Locate every blood parasite and identify its species.
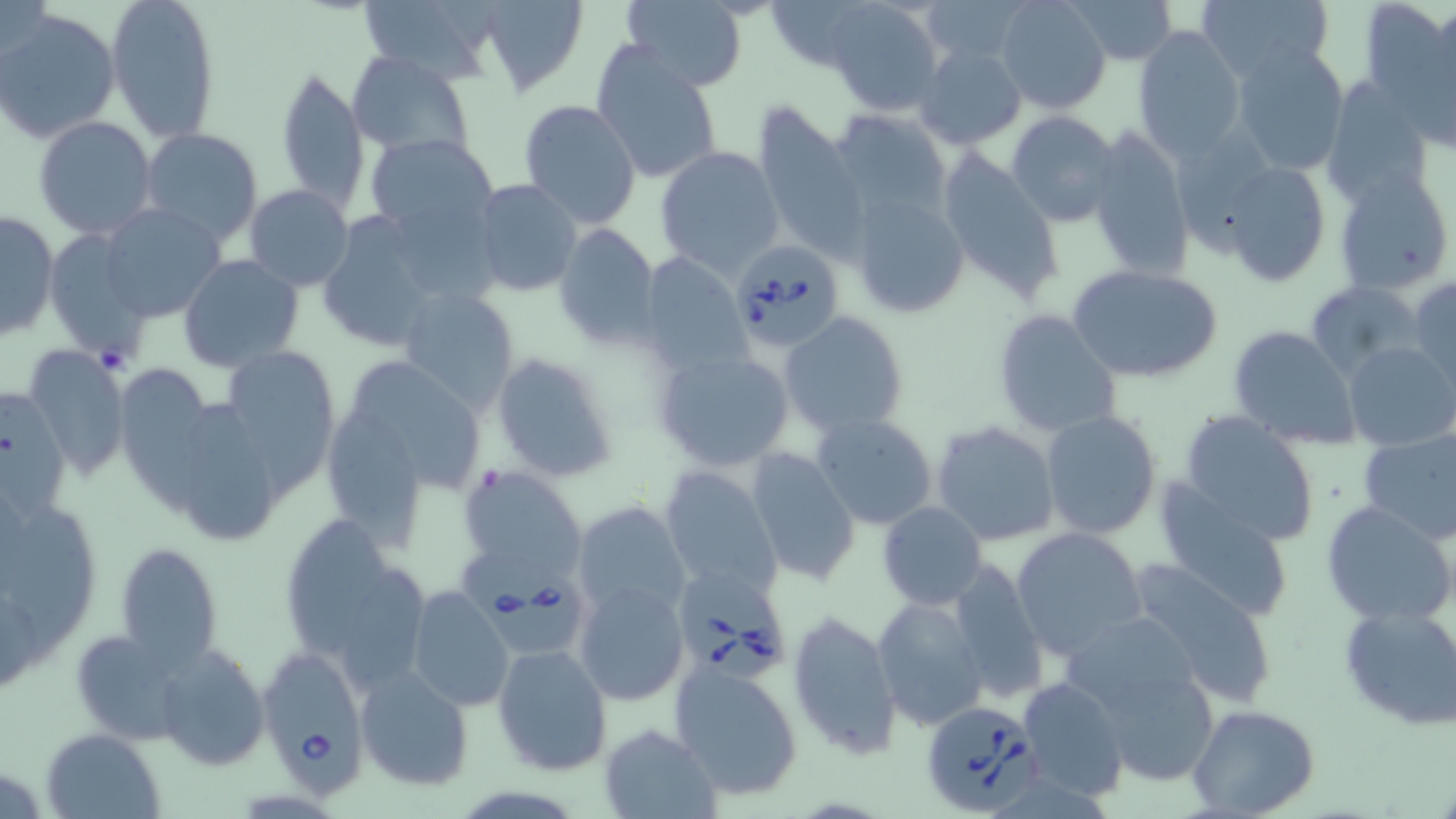
Approximate bounding boxes as (x1, y1, x2, y2) in pixels.
Babesia divergens-infected red blood cells: (733, 238, 844, 350), (460, 551, 604, 658), (680, 575, 790, 678), (257, 641, 372, 801), (919, 699, 1047, 817).
No Plasmodium falciparum, Plasmodium ovale, Plasmodium malariae, Plasmodium vivax, or Trypanosoma brucei observed.

Uninfected red blood cell locations: (0, 0, 56, 70), (105, 0, 221, 142), (357, 0, 496, 81), (476, 0, 588, 95), (618, 0, 751, 91), (761, 0, 881, 72), (918, 0, 1032, 64), (994, 0, 1112, 115), (1070, 0, 1179, 64), (1198, 0, 1335, 86), (1361, 0, 1453, 114), (825, 1, 942, 117), (2, 8, 122, 144), (1133, 27, 1246, 158), (1231, 42, 1352, 176), (591, 43, 723, 186), (915, 43, 1026, 149), (347, 51, 474, 160), (275, 64, 370, 214), (1322, 74, 1433, 205), (518, 100, 640, 229), (750, 101, 869, 260), (831, 106, 951, 218), (1007, 111, 1121, 228), (34, 116, 157, 239), (1086, 124, 1193, 281), (138, 127, 265, 248), (364, 133, 500, 243), (934, 146, 1064, 305), (653, 147, 784, 277), (1220, 159, 1333, 287), (1334, 171, 1454, 295), (472, 180, 583, 299), (244, 184, 354, 291), (847, 189, 971, 318), (99, 203, 226, 322), (313, 208, 473, 352), (1, 211, 60, 342), (552, 222, 662, 351), (41, 228, 153, 363), (638, 251, 752, 377), (178, 254, 304, 372), (1068, 266, 1221, 384), (1408, 276, 1456, 392), (1308, 279, 1421, 373), (398, 287, 520, 414), (991, 309, 1121, 438), (779, 310, 910, 436), (1228, 326, 1360, 449), (1343, 341, 1455, 449), (24, 343, 132, 480), (221, 347, 340, 485), (651, 347, 796, 473), (489, 351, 620, 484), (349, 356, 483, 498), (123, 373, 219, 518), (189, 410, 277, 539), (1040, 410, 1162, 538), (1177, 411, 1320, 548), (811, 412, 939, 531), (324, 415, 424, 555), (931, 419, 1061, 546), (1358, 433, 1456, 545), (745, 448, 861, 587), (458, 466, 586, 583), (659, 467, 782, 596), (0, 485, 103, 668), (1156, 486, 1294, 620), (1320, 500, 1455, 627), (876, 501, 987, 609), (571, 502, 689, 625), (275, 510, 419, 674), (1012, 527, 1147, 658), (114, 541, 224, 669), (945, 555, 1049, 703), (1121, 559, 1282, 705), (575, 581, 688, 706), (407, 586, 513, 713), (872, 596, 989, 730), (1337, 603, 1456, 731), (1062, 610, 1208, 723), (788, 611, 903, 759), (69, 628, 189, 744), (492, 644, 612, 774), (154, 646, 268, 770), (670, 664, 804, 799), (1094, 665, 1221, 786), (355, 666, 473, 790), (1017, 675, 1129, 802), (1189, 706, 1320, 819), (598, 723, 722, 817), (42, 729, 165, 818). Slide-level diagnosis: Babesia divergens. One field of a larger specimen. Image is 1456×819 pixels. Thin blood smear. May-Grünwald-Giemsa stain. Captured at 1000x magnification. Optical microscopy.